Report the malaria status of this cell.
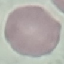

Uninfected.

Acquired by smartphone through the microscope eyepiece. Cell patch, automatically extracted from a larger field of view and resized to 64 × 64 pixels. Thin blood smear. Giemsa-stained preparation.